Give the position of every Plasmodium parasite visible.
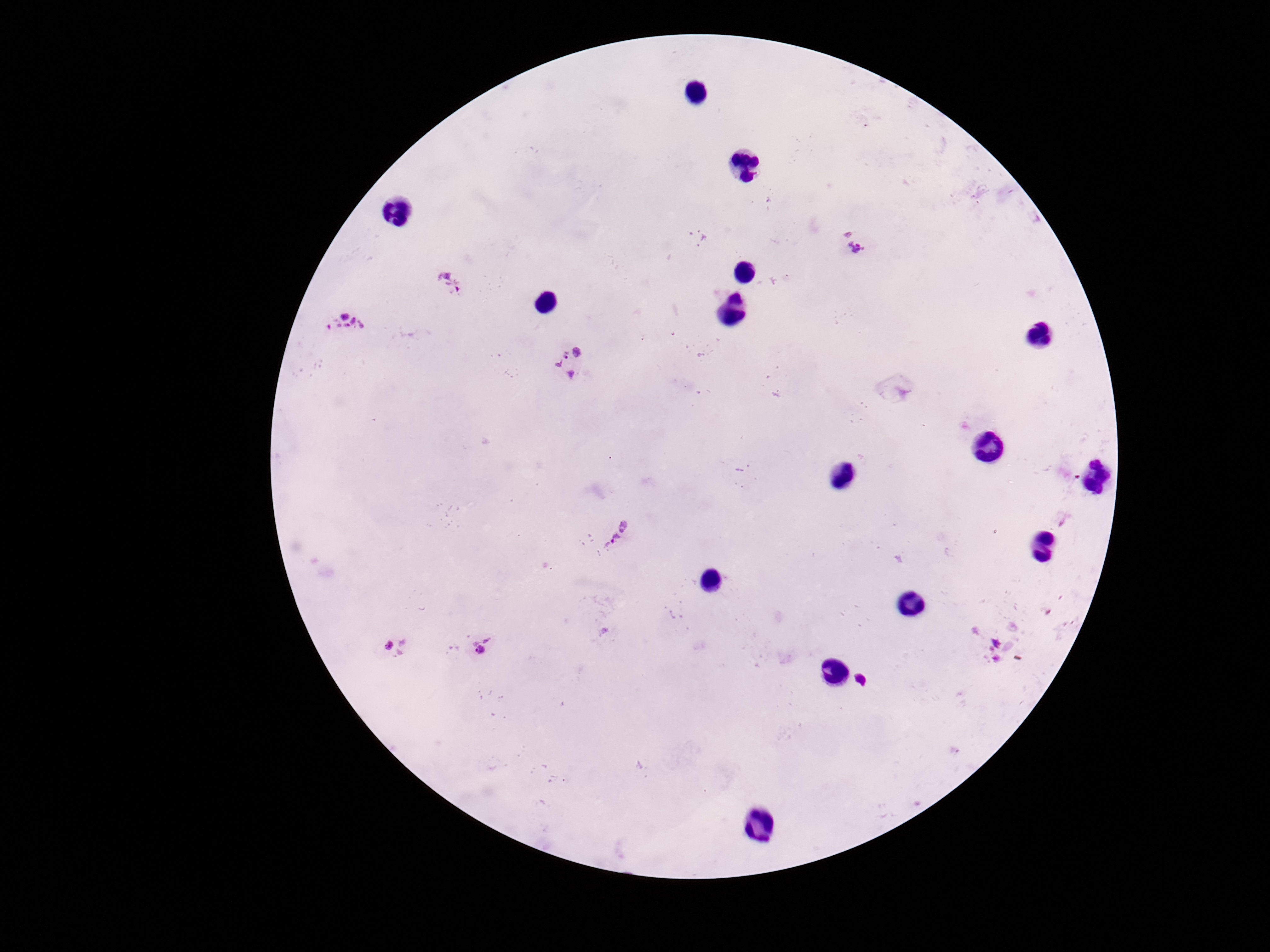
Approximate centers as {x, y} in pixels.
Plasmodium parasites: {699, 238}, {854, 240}, {449, 283}, {346, 321}, {571, 361}, {616, 535}, {395, 644}, {482, 644}.

Summary:
  - Stain: Giemsa
  - Preparation: thick blood smear
  - Capture: smartphone camera through the microscope eyepiece
  - Patient malaria status: positive
  - Image size: 1270×952 pixels
  - Magnification: 100x
  - Field of view: single